Give the extent of all uninfected red blood cells.
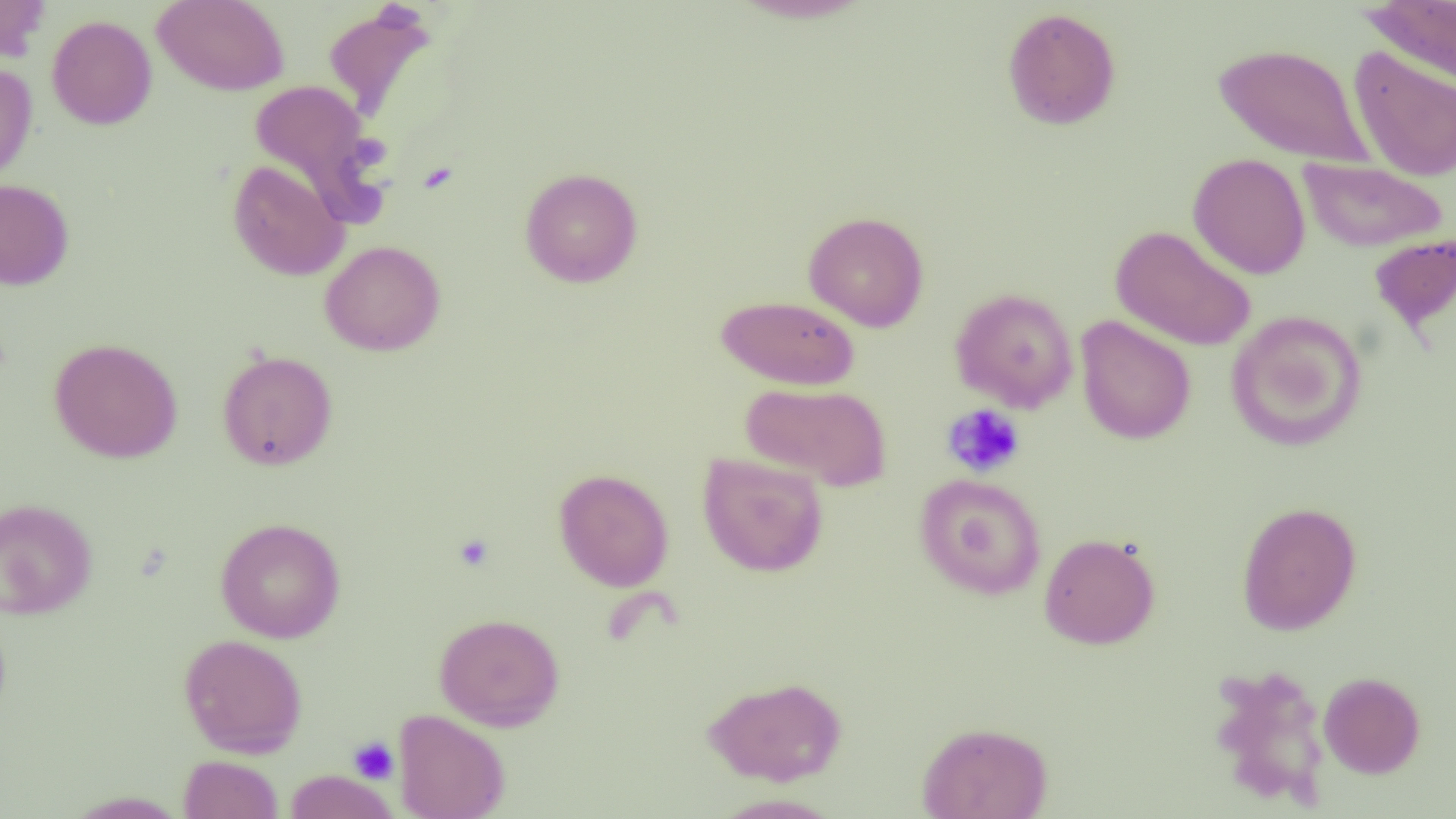
Approximate bounding boxes as [x1, y1, x2, y2] in pixels.
Uninfected red blood cells: [0, 0, 51, 63], [152, 0, 289, 96], [1361, 0, 1456, 88], [323, 5, 436, 124], [1002, 7, 1121, 131], [47, 15, 157, 130], [1213, 42, 1373, 168], [1348, 45, 1456, 183], [0, 62, 37, 185], [249, 80, 384, 219], [1188, 153, 1311, 279], [1299, 158, 1448, 252], [227, 159, 349, 281], [520, 167, 643, 287], [0, 178, 74, 290], [803, 211, 930, 332], [1110, 225, 1257, 351], [1368, 233, 1456, 335], [319, 240, 446, 356], [950, 288, 1079, 412], [716, 294, 859, 390], [1225, 309, 1367, 451], [1075, 315, 1196, 445], [49, 338, 183, 463], [217, 350, 338, 471], [740, 382, 892, 491], [697, 453, 829, 577], [553, 468, 674, 592], [915, 472, 1047, 600], [0, 498, 98, 620], [1236, 501, 1361, 636], [215, 517, 346, 643], [1038, 532, 1161, 649], [434, 612, 565, 731], [179, 633, 308, 758], [1208, 664, 1332, 808], [1318, 671, 1425, 778], [703, 675, 848, 786], [393, 709, 510, 819], [916, 721, 1053, 819], [179, 755, 284, 818], [284, 770, 399, 818], [62, 790, 191, 818], [709, 792, 843, 818].

slide_level_diagnosis: no evidence of blood parasites
magnification: 1000x
image_size: 1456×819 pixels
modality: light microscopy
field_of_view: one of a larger specimen
preparation: thin blood smear
platelet_locations: 'approximate bounding boxes as [x1, y1, x2, y2] in pixels: [941, 403, 1026, 478], [453, 533, 494, 571], [348, 736, 399, 784]'